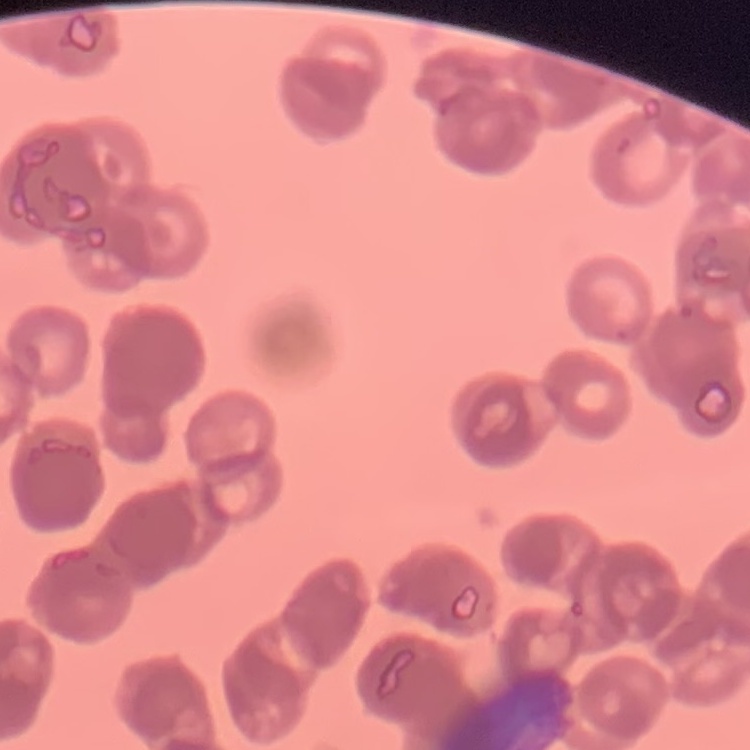

erythrocyte morphology = rouleaux formation
preparation = thin blood film
stain = Field's or Giemsa
image type = one tile cut from a larger photomicrograph